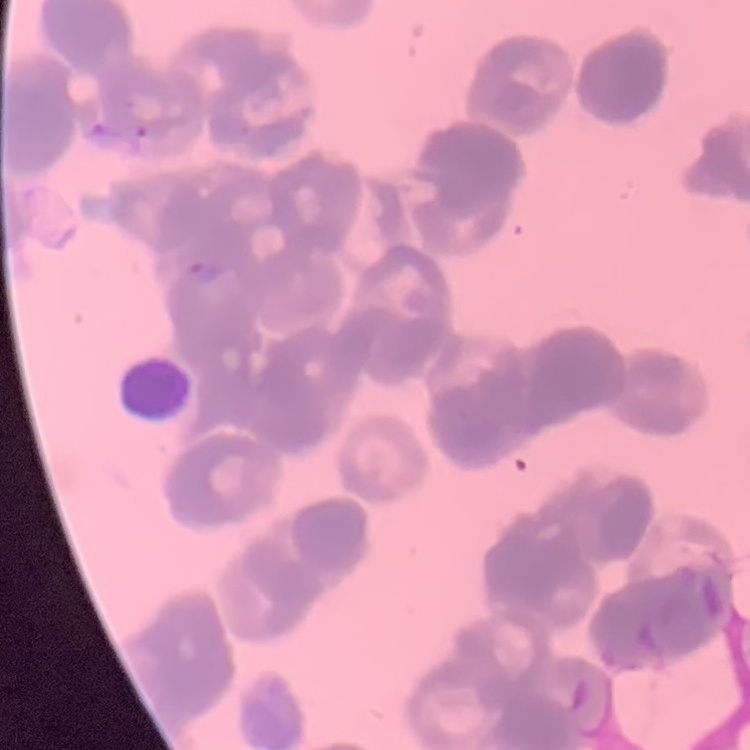

Summary:
  - Red blood cell morphology: rouleaux formation
  - Stain: Field's or Giemsa
  - Preparation: thin peripheral smear
  - Image type: one tile cut from a larger photomicrograph